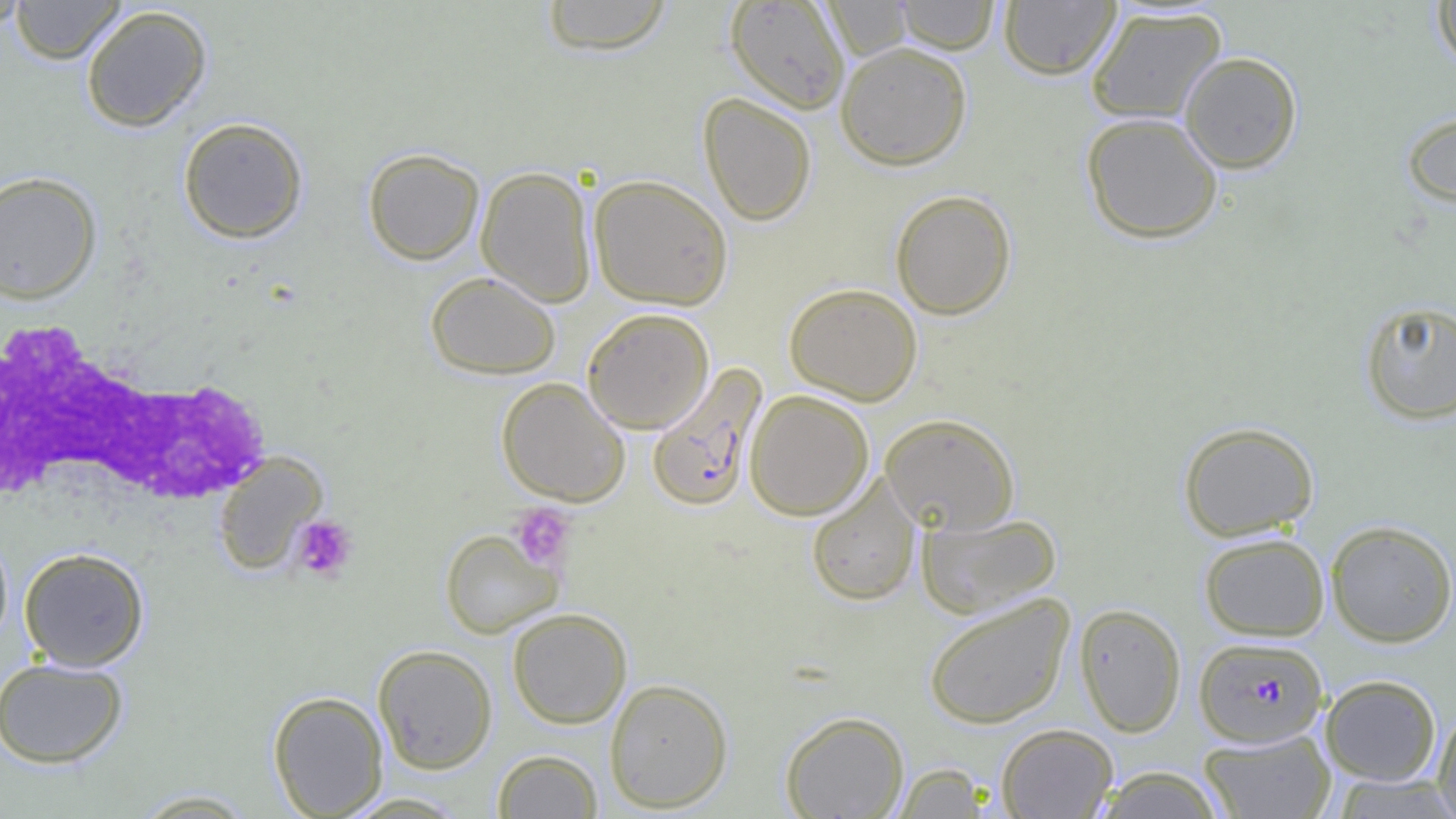
Summary:
  - Coordinate format: approximate bounding boxes as named x1/y1/x2/y2 corners in pixels
  - Plasmodium falciparum-infected red blood cell locations: (x1=646, y1=363, x2=768, y2=512), (x1=1194, y1=636, x2=1328, y2=747)
  - White blood cell locations: (x1=0, y1=316, x2=266, y2=515)
  - Uninfected red blood cell locations: (x1=0, y1=0, x2=32, y2=33), (x1=9, y1=0, x2=127, y2=64), (x1=540, y1=0, x2=674, y2=55), (x1=895, y1=0, x2=1000, y2=53), (x1=1430, y1=0, x2=1456, y2=73), (x1=725, y1=1, x2=850, y2=114), (x1=821, y1=1, x2=914, y2=59), (x1=998, y1=1, x2=1121, y2=80), (x1=80, y1=4, x2=213, y2=132), (x1=1085, y1=6, x2=1227, y2=125), (x1=835, y1=41, x2=972, y2=170), (x1=1179, y1=51, x2=1303, y2=174), (x1=698, y1=93, x2=816, y2=226), (x1=1400, y1=108, x2=1456, y2=210), (x1=1081, y1=112, x2=1223, y2=244), (x1=177, y1=117, x2=309, y2=244), (x1=362, y1=147, x2=484, y2=265), (x1=475, y1=166, x2=597, y2=306), (x1=0, y1=170, x2=102, y2=305), (x1=588, y1=174, x2=734, y2=310), (x1=890, y1=189, x2=1017, y2=319), (x1=425, y1=271, x2=561, y2=379), (x1=784, y1=283, x2=923, y2=405), (x1=1359, y1=299, x2=1456, y2=425), (x1=582, y1=307, x2=715, y2=434), (x1=496, y1=377, x2=631, y2=506), (x1=745, y1=390, x2=874, y2=520), (x1=880, y1=413, x2=1020, y2=534), (x1=1177, y1=420, x2=1319, y2=541), (x1=212, y1=450, x2=328, y2=575), (x1=806, y1=474, x2=921, y2=607), (x1=916, y1=511, x2=1063, y2=619), (x1=1325, y1=519, x2=1456, y2=647), (x1=439, y1=528, x2=563, y2=638), (x1=0, y1=529, x2=13, y2=651), (x1=1199, y1=532, x2=1330, y2=641), (x1=18, y1=547, x2=150, y2=671), (x1=923, y1=592, x2=1075, y2=729), (x1=1074, y1=602, x2=1187, y2=737), (x1=506, y1=608, x2=632, y2=728), (x1=373, y1=644, x2=497, y2=774), (x1=0, y1=656, x2=128, y2=769), (x1=1320, y1=674, x2=1441, y2=785), (x1=604, y1=678, x2=733, y2=812), (x1=268, y1=690, x2=388, y2=818), (x1=1432, y1=706, x2=1456, y2=817), (x1=780, y1=710, x2=909, y2=818), (x1=996, y1=723, x2=1118, y2=818), (x1=1198, y1=728, x2=1336, y2=819), (x1=492, y1=749, x2=604, y2=818), (x1=891, y1=763, x2=992, y2=818), (x1=1091, y1=766, x2=1226, y2=819), (x1=1329, y1=774, x2=1456, y2=818), (x1=129, y1=788, x2=260, y2=817), (x1=340, y1=792, x2=471, y2=818)
  - Platelet locations: (x1=508, y1=503, x2=576, y2=571), (x1=291, y1=513, x2=359, y2=583)
  - Slide-level diagnosis: Plasmodium falciparum
  - Modality: light microscopy
  - Magnification: 1000x
  - Field of view: one of a larger specimen
  - Image size: 1456×819 pixels
  - Preparation: thin blood smear